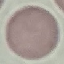 Malaria status: uninfected. Photographed with a smartphone camera at the microscope eyepiece. Cell patch, automatically extracted from a larger field of view and resized to 64 × 64 pixels. Thin blood smear. Giemsa-stained preparation.